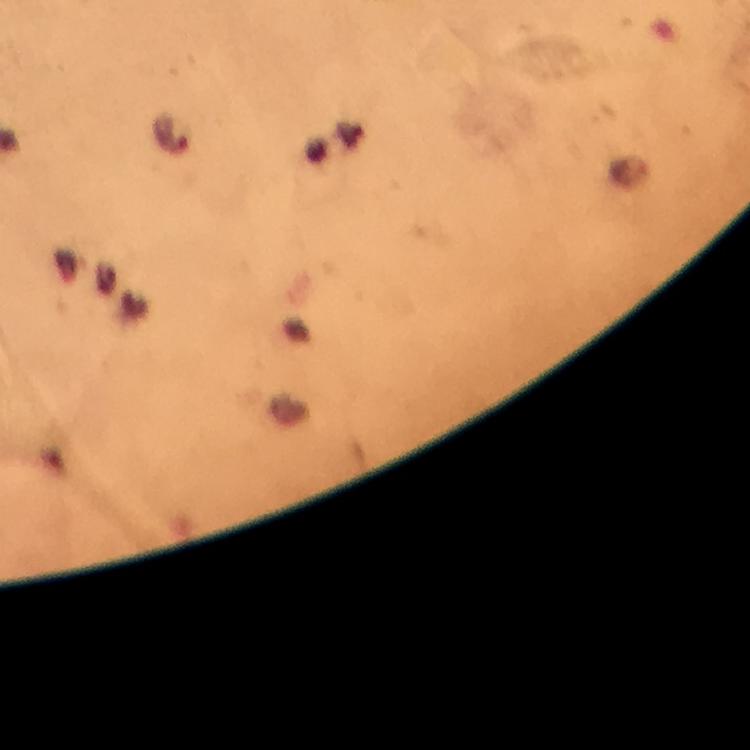

Approximate centers as [x, y] in pixels. Malaria parasite locations: [168, 133]. 100x magnification. From a malaria diagnostic workup. Immersion oil was used. Image is 750×750 pixels. Thick blood film. Giemsa stain. Photographed with a smartphone mounted on the microscope. A crop from one field of view.